Locate platelets.
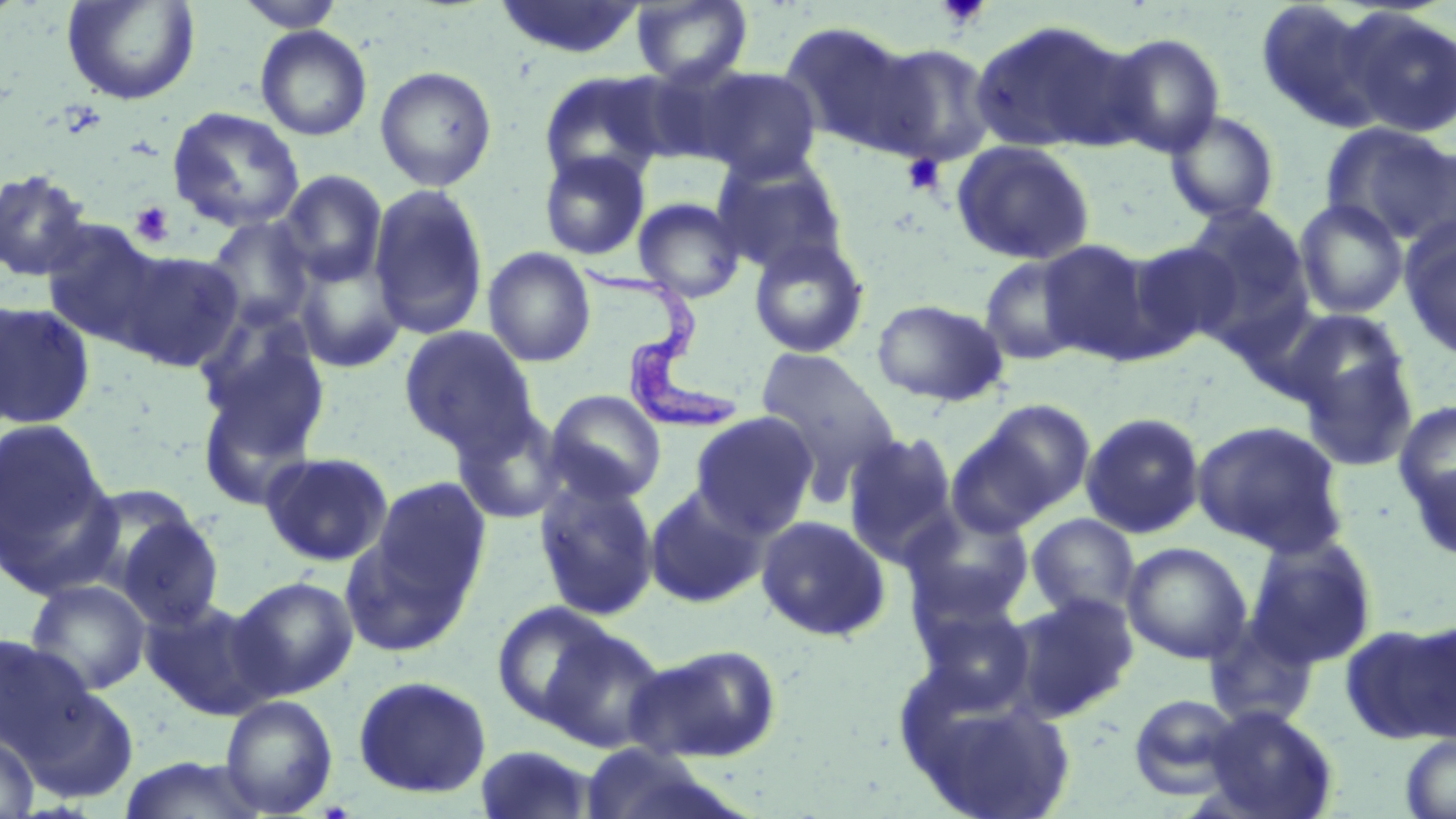
Approximate bounding boxes as (x1,y1)-(x2,y2) corner pairs in pixels.
Platelets: (936,1)-(991,31), (902,153)-(946,195), (129,201)-(175,248).

Uninfected red blood cell locations: (61,0)-(201,106), (234,0)-(345,32), (492,0)-(647,60), (630,0)-(754,87), (1254,1)-(1390,133), (1345,9)-(1456,138), (968,18)-(1138,155), (779,20)-(926,155), (255,25)-(372,141), (1101,32)-(1226,157), (867,41)-(1000,167), (375,65)-(497,191), (693,66)-(823,183), (538,71)-(669,189), (166,106)-(305,233), (1165,109)-(1281,224), (1321,122)-(1456,246), (950,139)-(1096,266), (538,150)-(651,261), (711,152)-(850,276), (0,168)-(93,282), (277,170)-(388,288), (368,183)-(489,341), (632,197)-(746,303), (1294,199)-(1409,319), (1182,203)-(1313,342), (203,216)-(317,330), (38,219)-(170,349), (1400,221)-(1456,360), (748,236)-(871,360), (1036,239)-(1158,362), (1123,239)-(1243,356), (483,247)-(596,368), (113,249)-(245,372), (292,250)-(408,374), (979,252)-(1091,365), (871,298)-(1009,406), (0,299)-(96,429), (193,308)-(332,476), (1279,308)-(1409,415), (399,325)-(538,453), (1293,336)-(1419,473), (754,347)-(902,493), (544,389)-(667,504), (954,398)-(1097,529), (1394,400)-(1456,520), (451,406)-(570,525), (690,411)-(819,538), (1080,411)-(1206,539), (1,418)-(113,576), (1192,419)-(1349,556), (842,430)-(960,567), (259,451)-(395,567), (1406,455)-(1456,563), (532,474)-(661,622), (368,478)-(490,603), (68,483)-(211,603), (644,483)-(770,609), (900,504)-(1037,626), (107,509)-(225,630), (1026,513)-(1140,621), (755,515)-(891,641), (339,526)-(477,658), (1244,535)-(1377,667), (1122,542)-(1252,664), (230,575)-(359,699), (25,579)-(152,696), (1009,592)-(1139,723), (141,596)-(277,719), (912,600)-(1038,712), (491,601)-(618,727), (1203,615)-(1320,730), (1341,620)-(1456,745), (541,624)-(670,753), (0,634)-(93,755), (626,643)-(782,763), (352,674)-(492,799), (19,684)-(141,804), (902,690)-(1078,819), (1128,693)-(1245,798), (219,695)-(338,817), (1202,706)-(1339,819), (0,734)-(38,818), (1400,734)-(1456,819), (474,744)-(599,819), (118,756)-(270,819). Trypanosoma brucei locations: (571,256)-(744,431). Slide-level diagnosis: Trypanosoma brucei. Image is 1456×819 pixels. 1000x magnification. Thin blood film. Light microscopy. May-Grünwald-Giemsa-stained preparation. Single field of view.